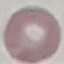
Malaria status: uninfected. Giemsa-stained preparation. Cell patch, automatically extracted from a larger field of view and resized to 64 × 64 pixels. Thin smear of blood. Acquired by smartphone through the microscope eyepiece.